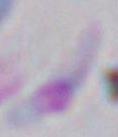 Micrograph. Toxoplasma gondii is shown. Captured at 1000x magnification.